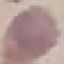 Malaria status: uninfected. Giemsa stain. Cell patch, automatically extracted from a larger field of view and resized to 64 × 64 pixels. Photographed with a smartphone camera at the microscope eyepiece. Thin smear of blood.